Assess this cell for malaria.
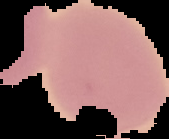
It is uninfected.

image size = 169×139 pixels
preparation = thin blood film
image type = segmented cell region with the area outside set to black